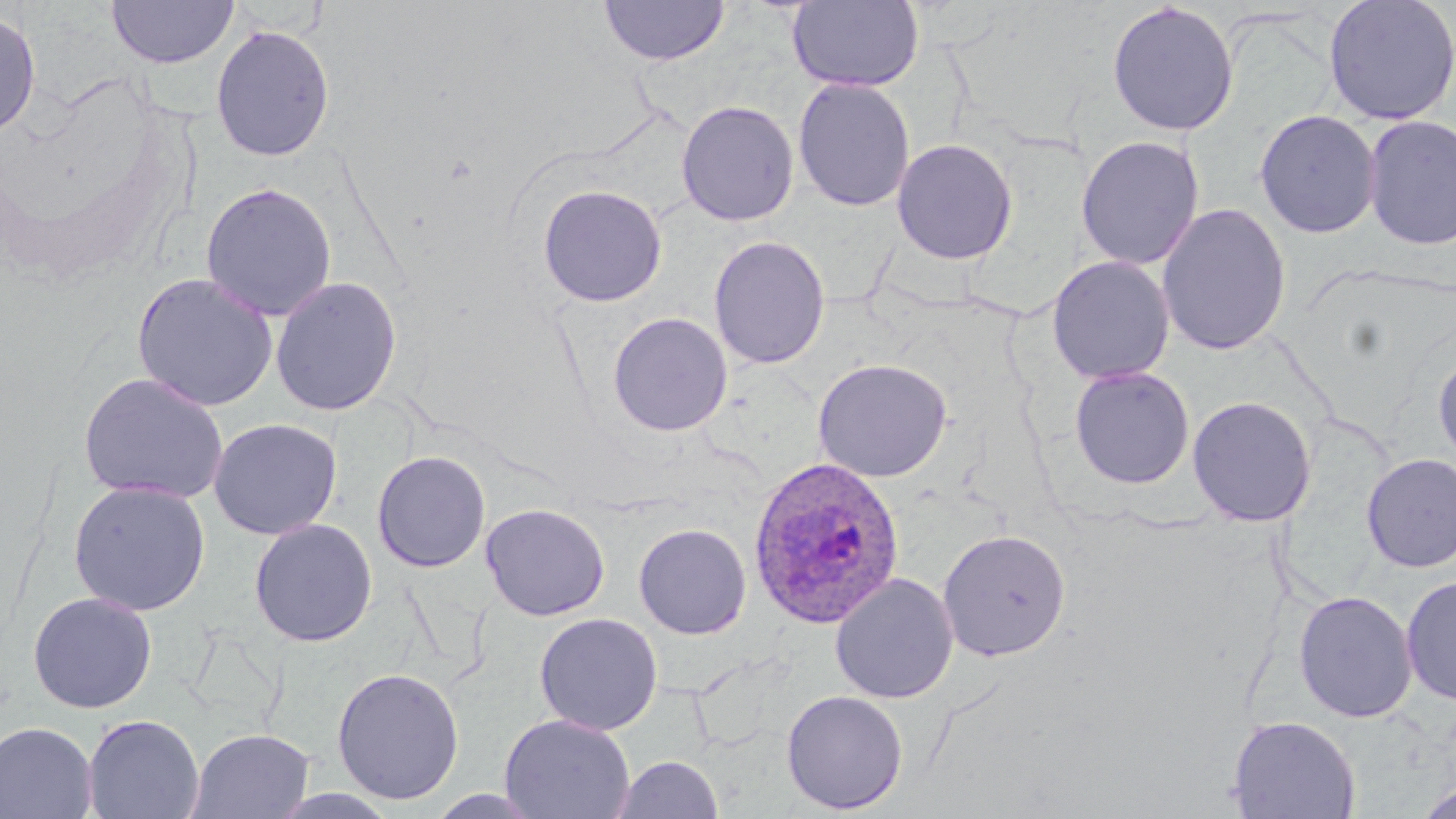

slide-level diagnosis = Plasmodium ovale
field of view = one of a larger specimen
modality = optical microscopy
stain = May-Grünwald-Giemsa
uninfected red blood cell locations = approximate bounding boxes as [x1, y1, x2, y2] in pixels: [598, 0, 730, 66], [787, 0, 924, 93], [1322, 0, 1455, 126], [106, 1, 238, 69], [1106, 1, 1240, 137], [0, 9, 41, 139], [210, 24, 335, 162], [792, 77, 915, 212], [676, 100, 800, 227], [1254, 109, 1381, 239], [1362, 114, 1456, 251], [1076, 135, 1205, 271], [891, 137, 1019, 265], [200, 182, 338, 321], [536, 184, 668, 308], [1156, 202, 1292, 356], [708, 235, 831, 370], [1046, 255, 1176, 384], [131, 272, 278, 411], [269, 275, 403, 416], [606, 312, 733, 437], [1432, 347, 1456, 468], [812, 358, 953, 483], [1069, 366, 1195, 489], [78, 371, 228, 505], [1187, 395, 1317, 527], [207, 417, 342, 540], [372, 450, 491, 573], [1360, 453, 1456, 572], [68, 479, 212, 616], [481, 503, 610, 621], [248, 518, 378, 647], [633, 522, 752, 639], [937, 529, 1071, 661], [829, 572, 959, 704], [1400, 575, 1456, 707], [1293, 590, 1418, 723], [27, 591, 158, 714], [534, 612, 663, 735], [331, 667, 465, 805], [780, 690, 908, 814], [499, 713, 635, 819], [82, 714, 205, 819], [1226, 715, 1361, 819], [0, 720, 98, 819], [186, 728, 314, 819], [610, 755, 724, 818], [1415, 782, 1456, 819], [426, 789, 548, 818]
preparation = thin blood film
magnification = 1000x
Plasmodium ovale-infected red blood cell locations = approximate bounding boxes as [x1, y1, x2, y2] in pixels: [747, 456, 905, 630]
image size = 1456×819 pixels